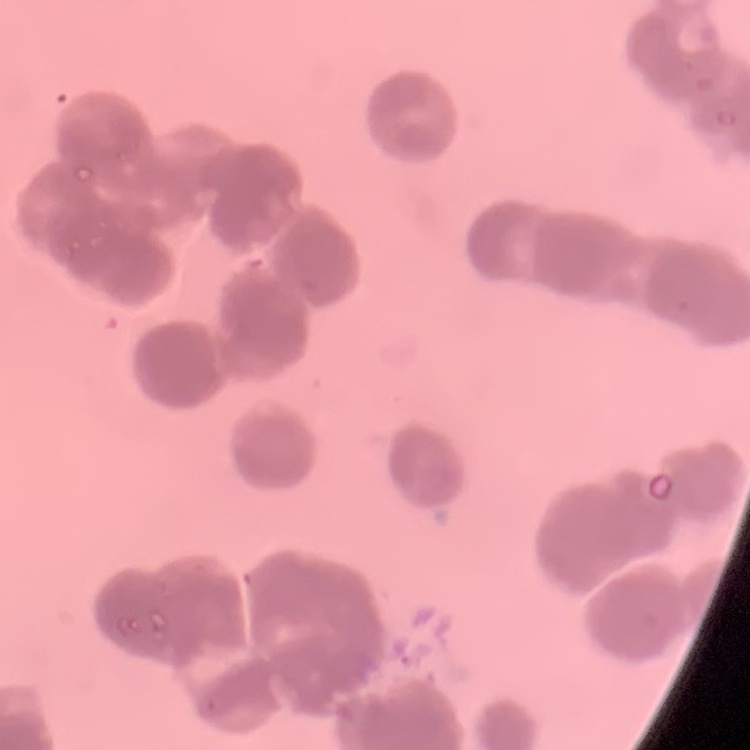

The erythrocytes show rouleaux formation. Square crop of a larger photomicrograph. Field's or Giemsa stain. Thin blood film.